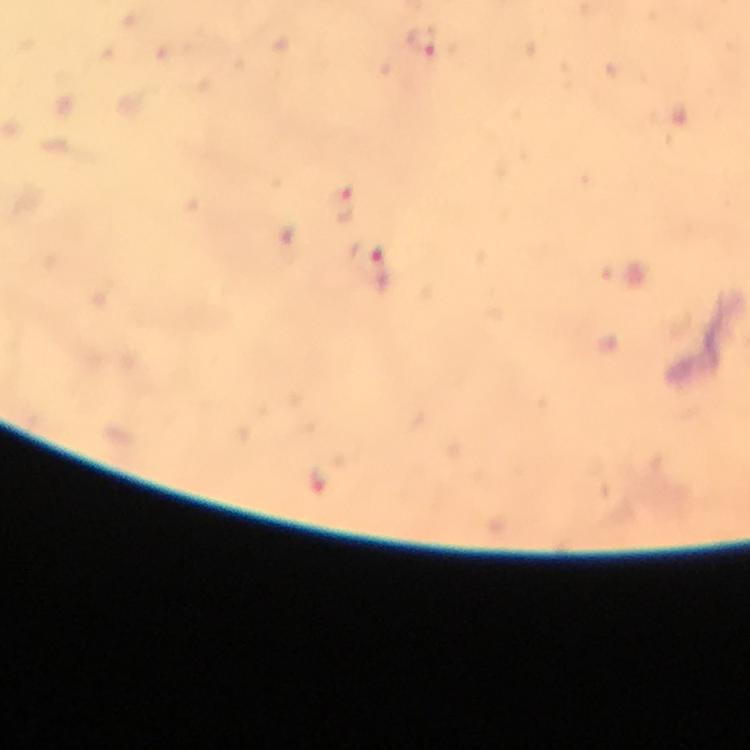

Approximate centers as (x, y) in pixels.
Summary:
  - Plasmodium parasite locations: (422, 41), (342, 205), (371, 267)
  - Magnification: 100x
  - Image size: 750×750 pixels
  - Context: from a diagnostic examination for malaria
  - Capture: smartphone photograph through a microscope
  - Cropped from: a single field of view
  - Stain: Giemsa
  - Immersion oil: applied
  - Preparation: thick blood film